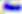
Photomicrograph. 400x magnification. Toxoplasma gondii is shown.